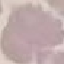
{
  "malaria_status": "uninfected",
  "stain": "Giemsa",
  "preparation": "thin blood film",
  "image_type": "cell patch, automatically extracted from a larger field of view and resized to 64 × 64 pixels",
  "capture": "smartphone camera at the microscope eyepiece"
}